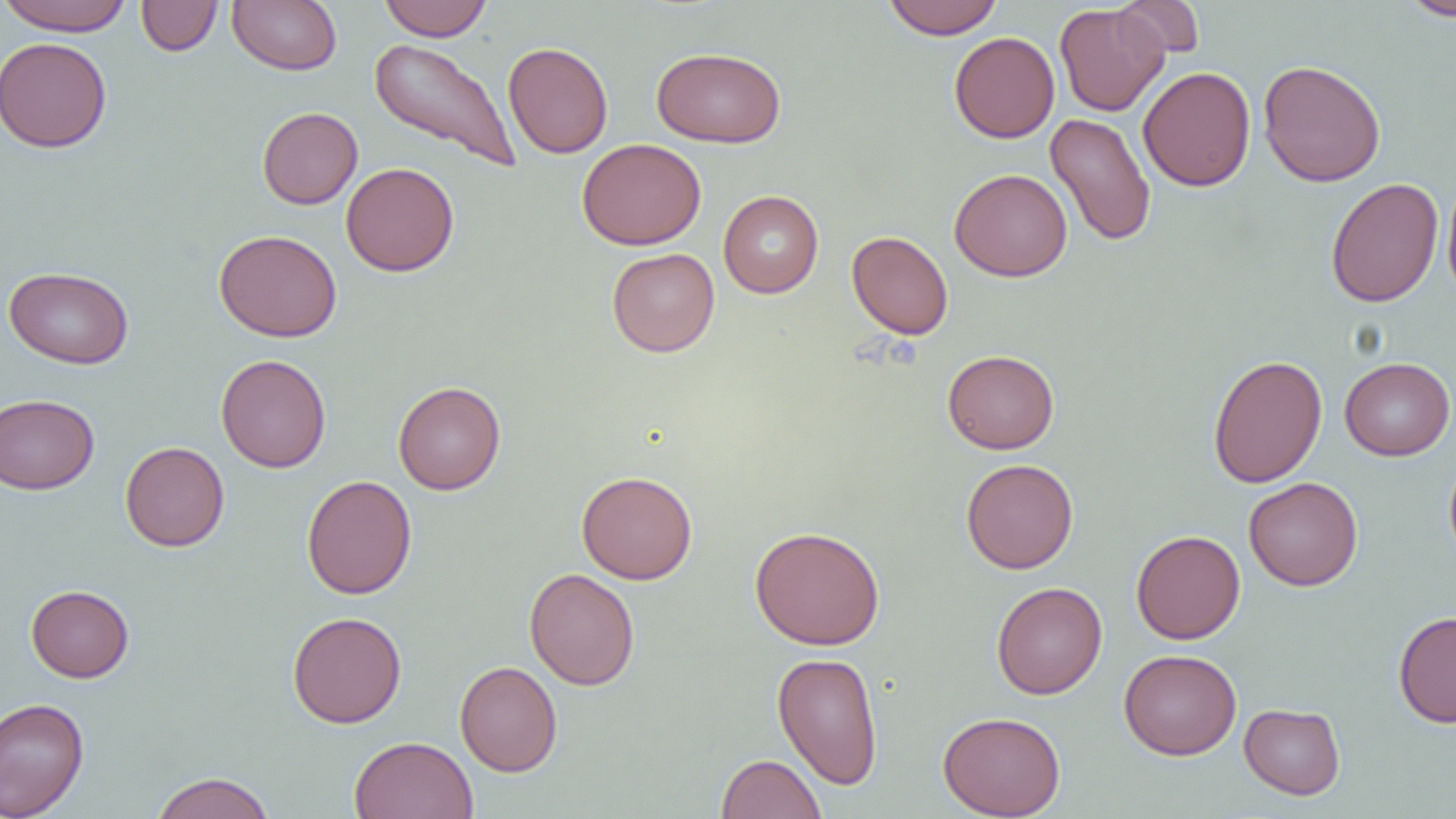
slide-level diagnosis = no evidence of blood parasites
magnification = 1000x
image size = 1456×819 pixels
preparation = thin blood film
modality = light microscopy
uninfected red blood cell locations = approximate bounding boxes as (x1, y1, x2, y2) in pixels: (0, 0, 134, 36), (136, 0, 222, 56), (228, 0, 342, 75), (379, 0, 492, 41), (882, 0, 1003, 40), (1112, 0, 1204, 62), (1398, 0, 1456, 21), (1054, 3, 1169, 117), (949, 31, 1060, 143), (0, 36, 112, 153), (369, 38, 521, 173), (503, 41, 613, 158), (652, 46, 786, 147), (1258, 59, 1385, 187), (1138, 67, 1256, 191), (257, 107, 363, 209), (1045, 113, 1156, 247), (576, 138, 706, 250), (341, 162, 459, 276), (949, 168, 1072, 282), (1442, 173, 1456, 304), (1325, 177, 1444, 308), (718, 190, 823, 298), (213, 229, 342, 342), (847, 231, 953, 340), (607, 248, 720, 357), (3, 266, 135, 369), (942, 349, 1059, 454), (215, 354, 331, 472), (1208, 354, 1327, 488), (1339, 357, 1455, 461), (393, 381, 506, 495), (0, 393, 99, 494), (120, 441, 230, 551), (1444, 453, 1456, 567), (961, 458, 1078, 574), (576, 470, 698, 584), (301, 474, 417, 600), (1244, 477, 1363, 590), (750, 526, 885, 650), (1131, 530, 1245, 644), (524, 568, 640, 690), (992, 581, 1107, 699), (25, 584, 134, 682), (1393, 610, 1456, 727), (287, 611, 407, 728), (1118, 649, 1242, 760), (772, 651, 884, 790), (455, 660, 563, 777), (0, 697, 90, 819), (1239, 703, 1345, 799), (938, 711, 1066, 818), (349, 736, 479, 819), (716, 753, 826, 819), (150, 771, 276, 819)
field of view = one of a larger specimen